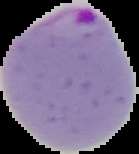
preparation = thin blood smear
image type = cell region segmented out of the field of view; surrounding area masked to black
result = malaria parasites detected
image size = 139×154 pixels